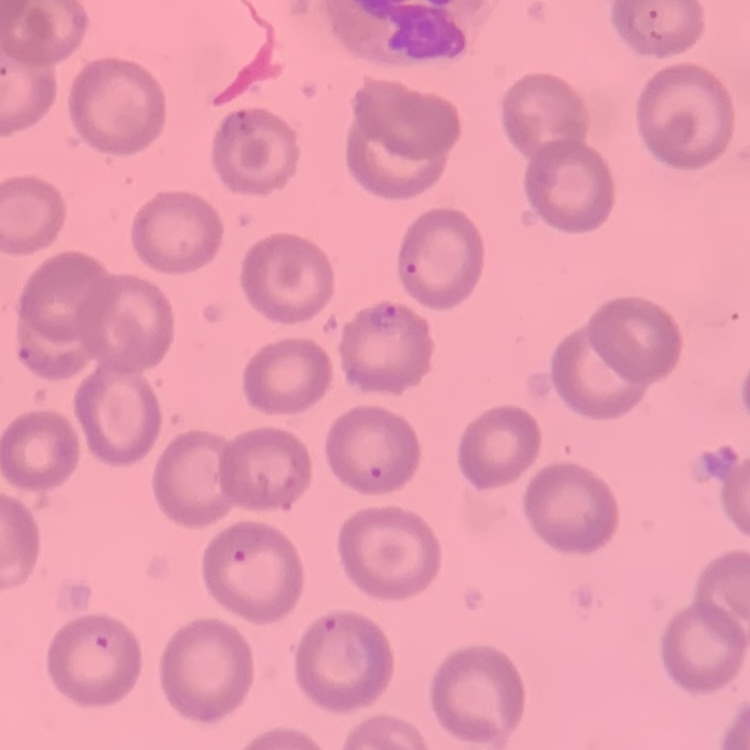

The erythrocytes show no rouleaux formation. One tile cut from a larger photomicrograph. Field's or Giemsa stain. Thin blood film.